Describe the morphology of the erythrocytes.
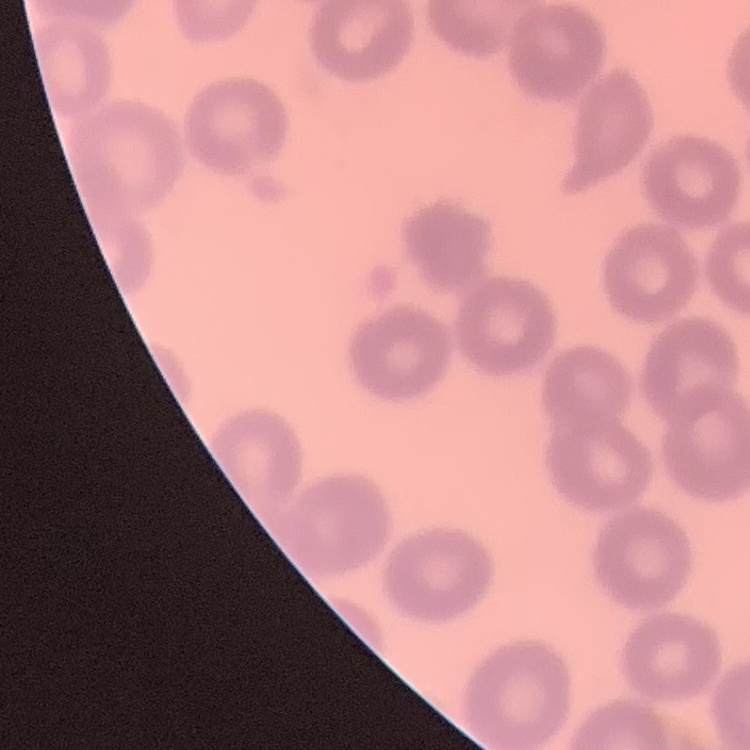

They show no rouleaux formation.

Thin peripheral smear. Square crop of a larger photomicrograph. Stained with either Field's or Giemsa.